Comment on the morphology of the erythrocytes.
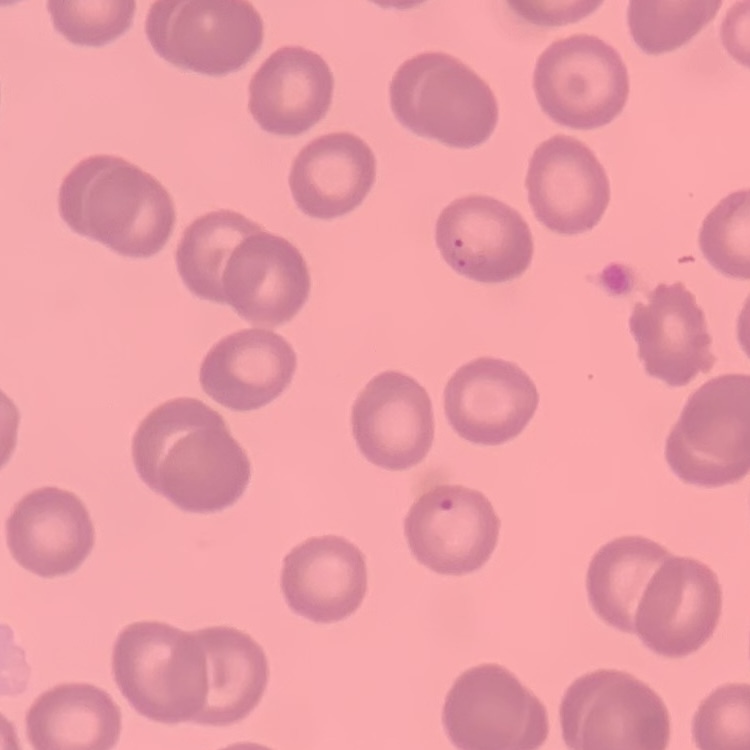

They show no rouleaux formation.

{
  "preparation": "thin blood film",
  "stain": "Field's or Giemsa",
  "image_type": "square crop of a larger photomicrograph"
}